Locate every uninfected red blood cell.
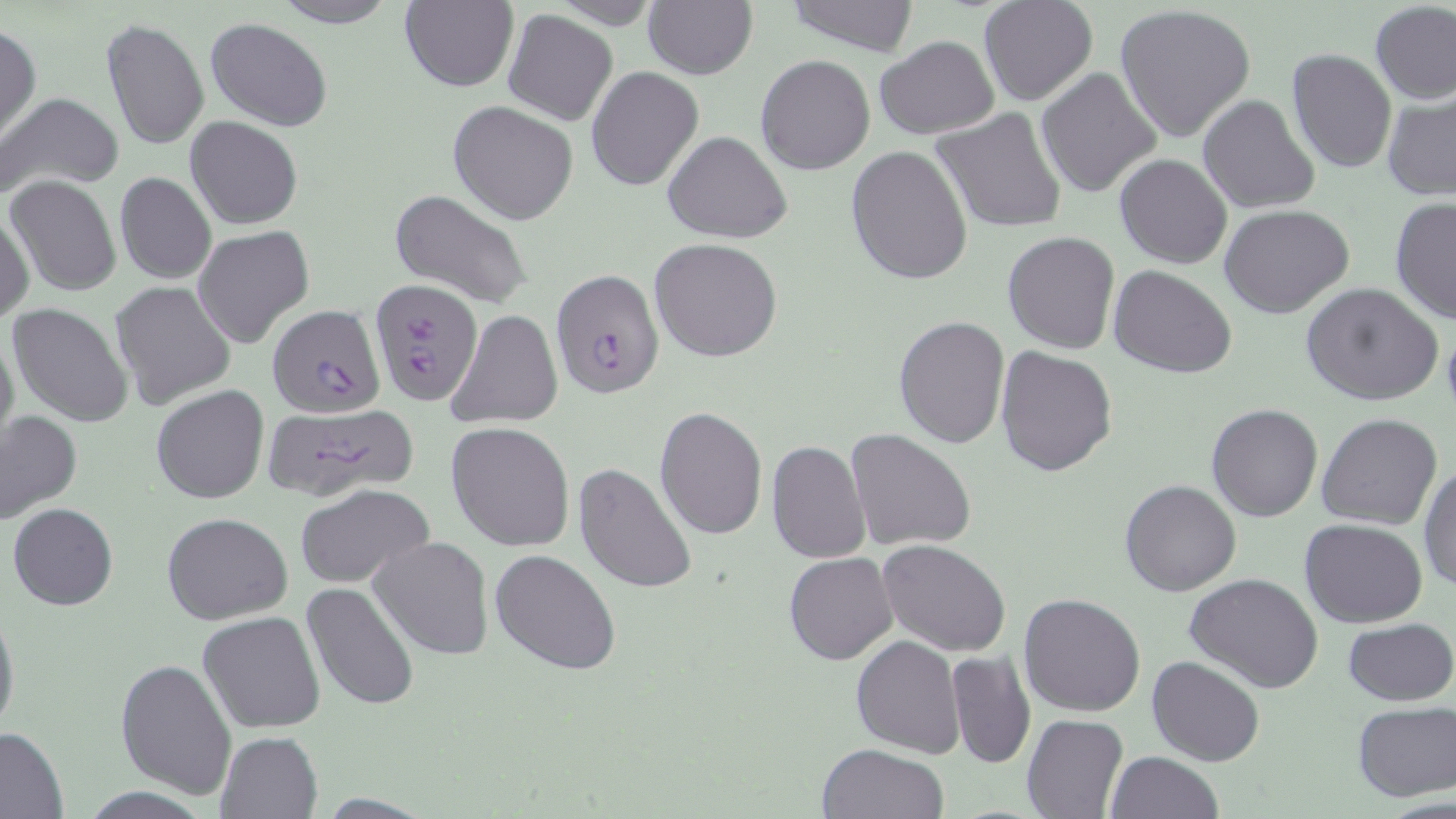

Approximate bounding boxes as [x1, y1, x2, y2] in pixels.
Uninfected red blood cells: [265, 0, 403, 27], [781, 0, 923, 55], [978, 0, 1099, 106], [399, 1, 518, 92], [644, 2, 756, 79], [1370, 3, 1456, 105], [1115, 4, 1258, 144], [503, 9, 618, 127], [100, 18, 209, 151], [205, 18, 332, 132], [0, 24, 40, 144], [873, 35, 1000, 139], [1286, 47, 1396, 173], [755, 55, 874, 175], [586, 67, 703, 190], [1037, 68, 1162, 198], [1381, 91, 1455, 201], [3, 94, 122, 196], [1197, 94, 1320, 214], [448, 100, 580, 225], [931, 108, 1068, 235], [185, 117, 303, 229], [664, 131, 791, 244], [845, 145, 973, 287], [1114, 154, 1232, 270], [114, 172, 216, 284], [7, 176, 121, 297], [389, 188, 533, 308], [1389, 198, 1455, 325], [1219, 204, 1354, 317], [1, 213, 36, 322], [193, 226, 314, 350], [1002, 230, 1120, 354], [648, 237, 784, 362], [1109, 266, 1237, 380], [109, 280, 236, 408], [1300, 282, 1445, 406], [8, 302, 132, 429], [445, 309, 562, 429], [894, 314, 1009, 448], [0, 324, 19, 458], [995, 344, 1115, 476], [152, 385, 270, 504], [1206, 402, 1324, 521], [654, 405, 769, 541], [0, 410, 83, 522], [1316, 413, 1442, 531], [447, 422, 575, 551], [845, 428, 978, 553], [765, 440, 872, 565], [573, 462, 698, 595], [1420, 464, 1456, 593], [1120, 478, 1242, 597], [295, 482, 435, 588], [9, 502, 119, 610], [162, 512, 294, 624], [1300, 518, 1427, 629], [370, 536, 493, 660], [878, 539, 1012, 657], [490, 550, 621, 677], [783, 551, 898, 665], [1184, 572, 1323, 694], [301, 582, 419, 711], [1018, 593, 1146, 716], [0, 602, 19, 744], [197, 611, 328, 733], [1342, 618, 1456, 706], [851, 635, 964, 757], [945, 651, 1036, 769], [1146, 656, 1266, 766], [116, 658, 237, 800], [1351, 701, 1456, 802], [1022, 714, 1129, 819], [0, 726, 68, 818], [215, 731, 323, 818], [815, 743, 949, 819], [1105, 752, 1223, 819].

slide-level diagnosis = Plasmodium falciparum
modality = optical microscopy
field of view = single
preparation = thin blood smear
Plasmodium falciparum-infected red blood cell locations = approximate bounding boxes as [x1, y1, x2, y2] in pixels: [549, 269, 664, 399], [371, 279, 483, 406], [268, 305, 383, 418], [261, 402, 421, 502]
image size = 1456×819 pixels
magnification = 1000x
stain = May-Grünwald-Giemsa